State which parasite is depicted.
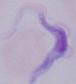
This is a trypanosome.

Summary:
  - Magnification: 1000x
  - Modality: photomicrograph